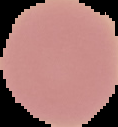
Result: no Plasmodium parasites seen. Image is 118×127 pixels. From a thin blood film. The area outside the segmented cell region is set to black.